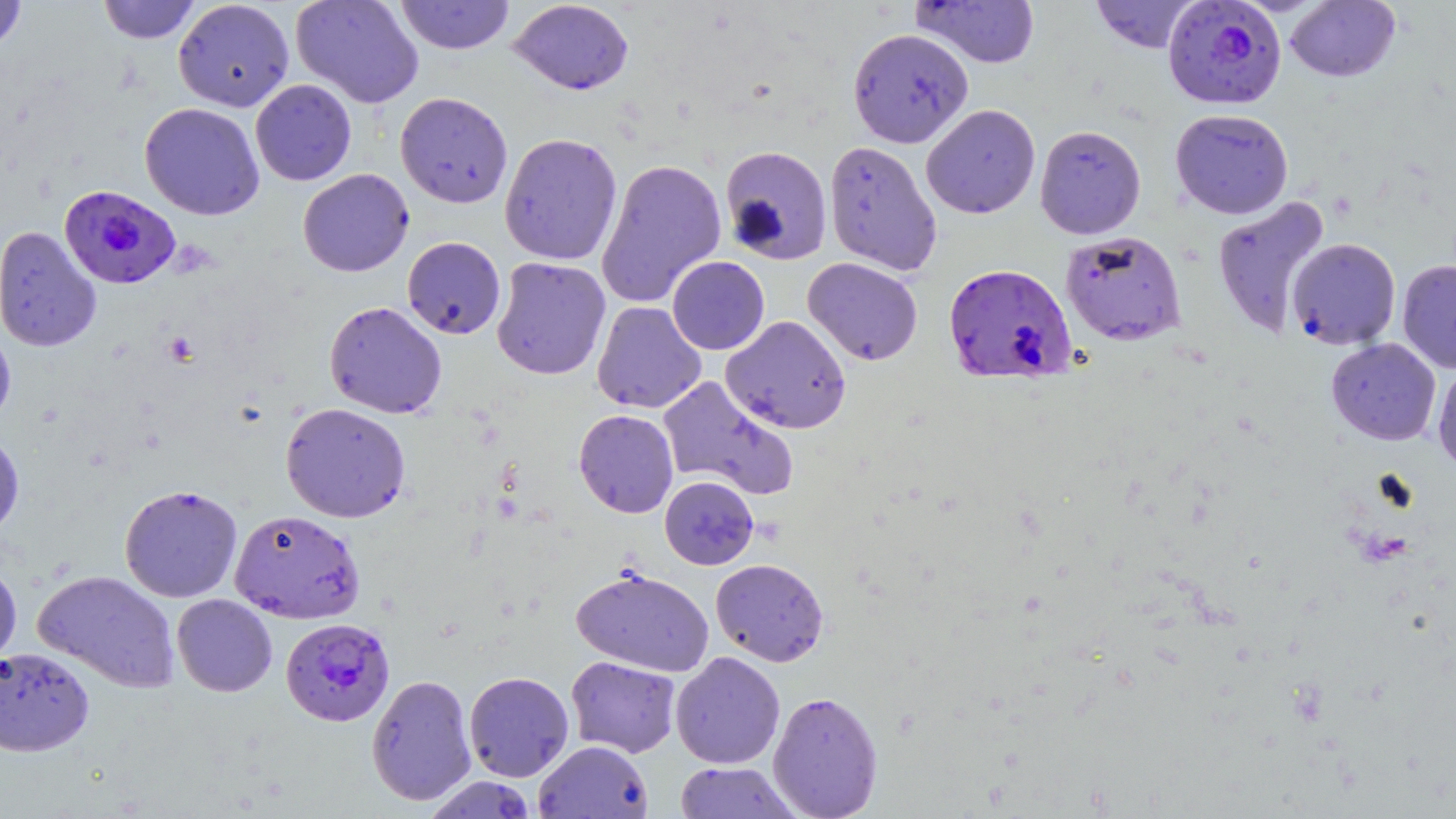

slide-level diagnosis = Plasmodium falciparum
preparation = thin blood smear
image size = 1456×819 pixels
stain = May-Grünwald-Giemsa
magnification = 1000x
Plasmodium falciparum-infected red blood cell locations = approximate bounding boxes as [x1, y1, x2, y2] in pixels: [1162, 0, 1287, 109], [59, 185, 180, 289], [944, 262, 1077, 384], [281, 617, 395, 726]
uninfected red blood cell locations = approximate bounding boxes as [x1, y1, x2, y2] in pixels: [0, 0, 28, 55], [97, 0, 202, 44], [173, 0, 295, 112], [290, 0, 425, 108], [395, 0, 515, 55], [508, 0, 634, 95], [1090, 0, 1201, 53], [912, 1, 1041, 68], [1285, 1, 1400, 82], [847, 27, 973, 148], [250, 79, 357, 186], [395, 91, 513, 208], [139, 102, 265, 220], [921, 103, 1040, 219], [1170, 108, 1294, 219], [1034, 124, 1147, 239], [499, 132, 622, 266], [823, 140, 943, 276], [719, 145, 833, 265], [595, 158, 727, 308], [298, 169, 414, 277], [1211, 196, 1330, 339], [0, 226, 102, 352], [1060, 230, 1186, 345], [402, 236, 506, 339], [1287, 237, 1401, 350], [491, 256, 611, 381], [667, 256, 770, 355], [803, 257, 923, 365], [1396, 259, 1456, 373], [324, 301, 447, 418], [592, 301, 706, 414], [721, 315, 852, 434], [0, 325, 16, 430], [1326, 337, 1441, 445], [1432, 363, 1456, 473], [656, 375, 800, 500], [280, 402, 411, 523], [573, 409, 679, 518], [0, 431, 24, 540], [659, 476, 758, 570], [119, 484, 243, 603], [229, 509, 365, 624], [710, 558, 829, 667], [0, 559, 22, 669], [571, 567, 714, 678], [32, 569, 181, 693], [171, 594, 277, 697], [0, 646, 94, 756], [670, 651, 785, 769], [566, 655, 681, 758], [463, 671, 574, 782], [366, 673, 477, 806], [767, 690, 884, 818], [534, 741, 652, 818], [674, 761, 800, 819], [424, 775, 539, 818]
modality = light microscopy
field of view = single